Describe the morphology of the erythrocytes.
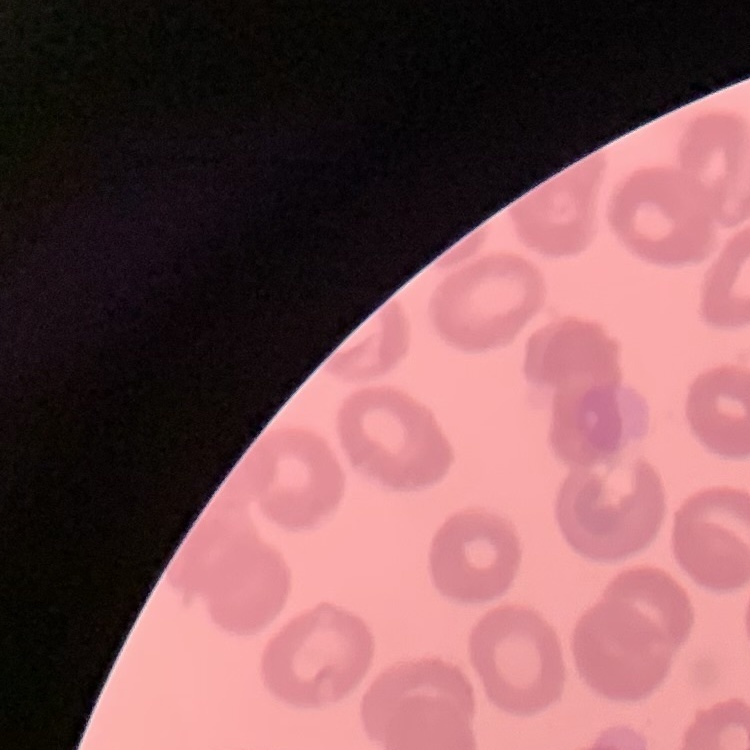
No rouleaux formation.

Field's or Giemsa stain. Thin blood smear. One tile cut from a larger photomicrograph.